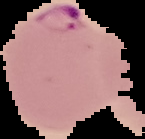 Image is 145×139 pixels. Result: Plasmodium parasites identified. Segmented cell region on a black background. From a thin blood film.